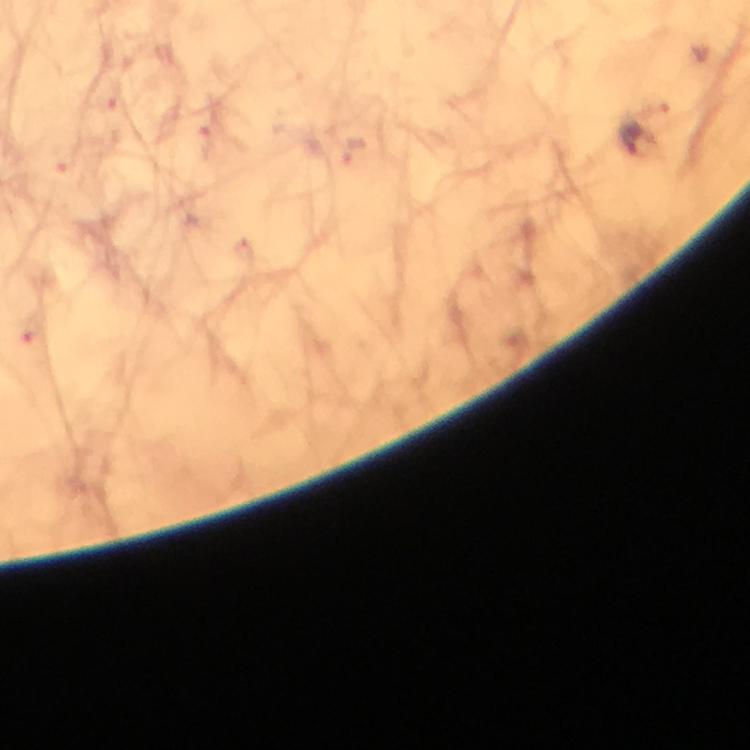

{
  "cropped_from": "one field of view",
  "magnification": "100x",
  "capture": "smartphone mounted on the microscope",
  "image_size": "750×750 pixels",
  "stain": "Giemsa",
  "context": "from a malaria diagnostic workup",
  "immersion_oil": "used",
  "preparation": "thick smear",
  "plasmodium_parasite_locations": "approximate centers as [x, y] in pixels: [630, 137], [29, 333]"
}